Locate every Plasmodium vivax-infected red blood cell.
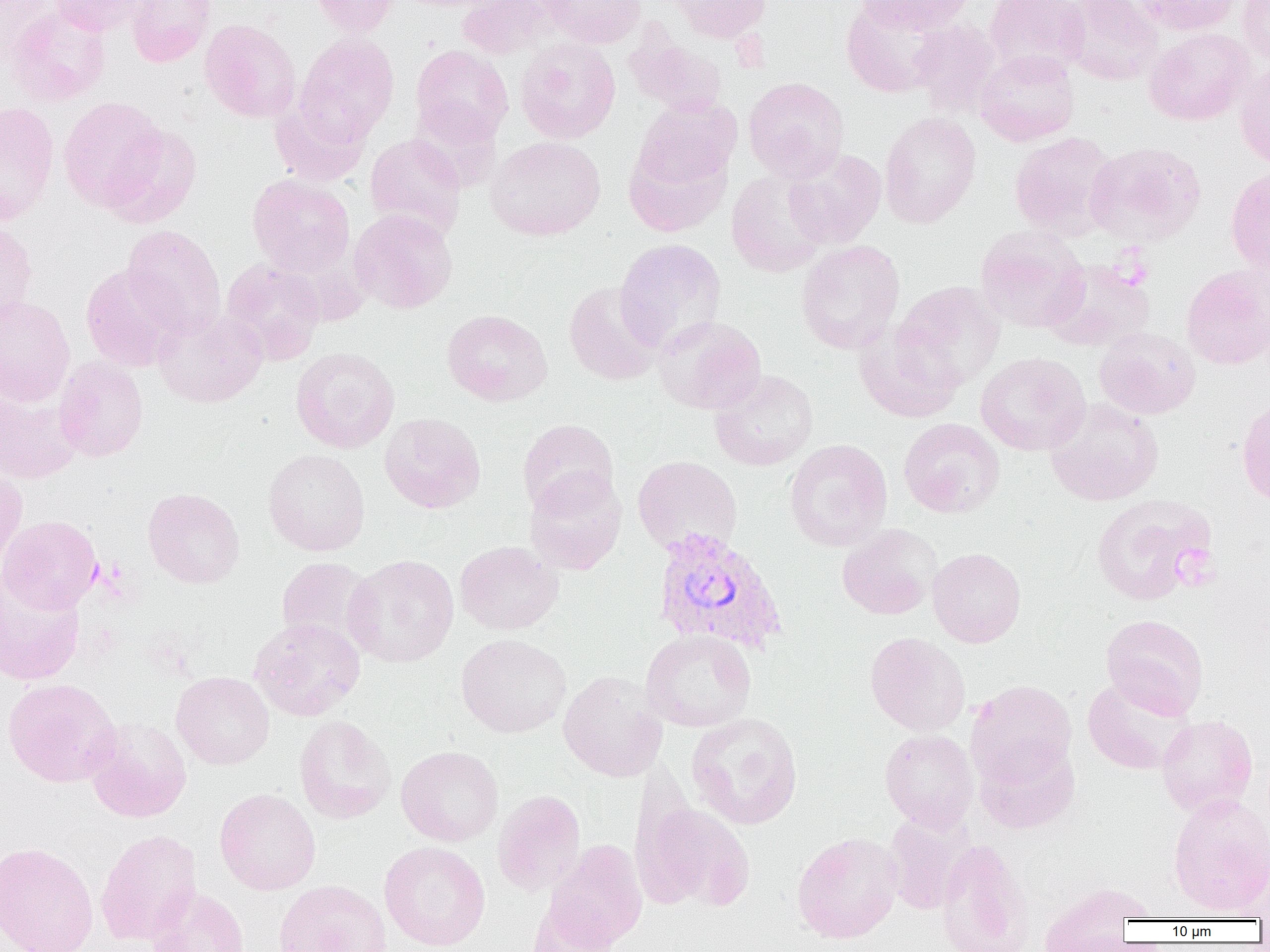

Approximate bounding boxes as named x1/y1/x2/y2 corners in pixels.
Plasmodium vivax-infected red blood cells: (x1=650, y1=527, x2=788, y2=656).

slide-level diagnosis = Plasmodium vivax
uninfected red blood cell locations = approximate bounding boxes as named x1/y1/x2/y2 corners in pixels: (x1=0, y1=0, x2=58, y2=64), (x1=47, y1=0, x2=149, y2=35), (x1=125, y1=0, x2=216, y2=67), (x1=309, y1=0, x2=399, y2=37), (x1=458, y1=0, x2=555, y2=59), (x1=537, y1=0, x2=646, y2=48), (x1=669, y1=0, x2=772, y2=43), (x1=855, y1=0, x2=974, y2=34), (x1=985, y1=0, x2=1089, y2=77), (x1=1061, y1=0, x2=1163, y2=85), (x1=1131, y1=0, x2=1242, y2=35), (x1=1237, y1=0, x2=1270, y2=65), (x1=841, y1=1, x2=949, y2=97), (x1=6, y1=6, x2=110, y2=107), (x1=200, y1=19, x2=301, y2=123), (x1=910, y1=20, x2=1002, y2=116), (x1=1144, y1=28, x2=1255, y2=125), (x1=625, y1=33, x2=727, y2=117), (x1=294, y1=34, x2=399, y2=144), (x1=515, y1=38, x2=621, y2=144), (x1=410, y1=45, x2=513, y2=146), (x1=974, y1=49, x2=1079, y2=146), (x1=1234, y1=62, x2=1270, y2=169), (x1=743, y1=77, x2=849, y2=182), (x1=58, y1=97, x2=168, y2=211), (x1=633, y1=98, x2=741, y2=193), (x1=269, y1=100, x2=369, y2=186), (x1=0, y1=101, x2=59, y2=225), (x1=408, y1=101, x2=502, y2=192), (x1=879, y1=112, x2=981, y2=228), (x1=104, y1=124, x2=202, y2=228), (x1=1009, y1=132, x2=1119, y2=238), (x1=364, y1=133, x2=467, y2=241), (x1=623, y1=134, x2=733, y2=238), (x1=486, y1=135, x2=606, y2=240), (x1=1085, y1=141, x2=1206, y2=246), (x1=783, y1=148, x2=887, y2=249), (x1=1225, y1=165, x2=1270, y2=275), (x1=727, y1=171, x2=829, y2=276), (x1=247, y1=174, x2=355, y2=277), (x1=349, y1=209, x2=458, y2=313), (x1=0, y1=220, x2=38, y2=324), (x1=122, y1=225, x2=226, y2=339), (x1=975, y1=225, x2=1089, y2=333), (x1=614, y1=238, x2=726, y2=355), (x1=796, y1=240, x2=905, y2=354), (x1=221, y1=259, x2=326, y2=365), (x1=1042, y1=259, x2=1155, y2=352), (x1=80, y1=264, x2=184, y2=372), (x1=1181, y1=264, x2=1270, y2=370), (x1=893, y1=280, x2=1006, y2=390), (x1=564, y1=281, x2=664, y2=385), (x1=0, y1=295, x2=75, y2=406), (x1=153, y1=308, x2=267, y2=408), (x1=442, y1=309, x2=552, y2=406), (x1=654, y1=316, x2=766, y2=415), (x1=854, y1=322, x2=966, y2=423), (x1=1094, y1=326, x2=1200, y2=420), (x1=290, y1=347, x2=400, y2=453), (x1=975, y1=352, x2=1091, y2=456), (x1=54, y1=356, x2=149, y2=462), (x1=710, y1=369, x2=818, y2=471), (x1=0, y1=383, x2=82, y2=484), (x1=1237, y1=396, x2=1270, y2=506), (x1=1044, y1=398, x2=1163, y2=505), (x1=379, y1=413, x2=485, y2=513), (x1=898, y1=417, x2=1005, y2=518), (x1=517, y1=419, x2=619, y2=517), (x1=784, y1=439, x2=893, y2=551), (x1=263, y1=448, x2=370, y2=556), (x1=632, y1=455, x2=743, y2=557), (x1=0, y1=464, x2=27, y2=571), (x1=525, y1=470, x2=626, y2=575), (x1=143, y1=488, x2=245, y2=588), (x1=1091, y1=493, x2=1216, y2=605), (x1=0, y1=515, x2=102, y2=613), (x1=837, y1=523, x2=942, y2=620), (x1=454, y1=540, x2=563, y2=635), (x1=927, y1=548, x2=1026, y2=648), (x1=343, y1=554, x2=459, y2=667), (x1=276, y1=557, x2=378, y2=652), (x1=0, y1=570, x2=86, y2=686), (x1=1101, y1=614, x2=1209, y2=719), (x1=249, y1=617, x2=365, y2=721), (x1=641, y1=629, x2=757, y2=732), (x1=865, y1=632, x2=970, y2=736), (x1=456, y1=633, x2=571, y2=738), (x1=171, y1=671, x2=274, y2=770), (x1=558, y1=671, x2=667, y2=781), (x1=1082, y1=676, x2=1196, y2=775), (x1=2, y1=678, x2=122, y2=787), (x1=966, y1=679, x2=1077, y2=786), (x1=686, y1=712, x2=803, y2=830), (x1=1157, y1=715, x2=1258, y2=816), (x1=294, y1=716, x2=396, y2=824), (x1=84, y1=717, x2=192, y2=822), (x1=879, y1=729, x2=979, y2=831), (x1=974, y1=739, x2=1080, y2=834), (x1=396, y1=745, x2=503, y2=846), (x1=215, y1=788, x2=321, y2=895), (x1=492, y1=789, x2=586, y2=897), (x1=1167, y1=793, x2=1270, y2=916), (x1=633, y1=799, x2=756, y2=913), (x1=882, y1=812, x2=975, y2=915), (x1=95, y1=829, x2=203, y2=946), (x1=792, y1=831, x2=903, y2=944), (x1=936, y1=838, x2=1034, y2=952), (x1=0, y1=841, x2=99, y2=952), (x1=379, y1=841, x2=491, y2=951), (x1=544, y1=841, x2=648, y2=949), (x1=273, y1=879, x2=392, y2=952), (x1=1036, y1=881, x2=1151, y2=951), (x1=144, y1=886, x2=249, y2=952), (x1=527, y1=900, x2=620, y2=952)
image size = 1270×952 pixels
modality = optical microscopy
field of view = one of a larger specimen
platelet locations = approximate bounding boxes as named x1/y1/x2/y2 corners in pixels: (x1=1111, y1=250, x2=1153, y2=288), (x1=1173, y1=546, x2=1217, y2=590)
magnification = 1000x
preparation = thin blood smear